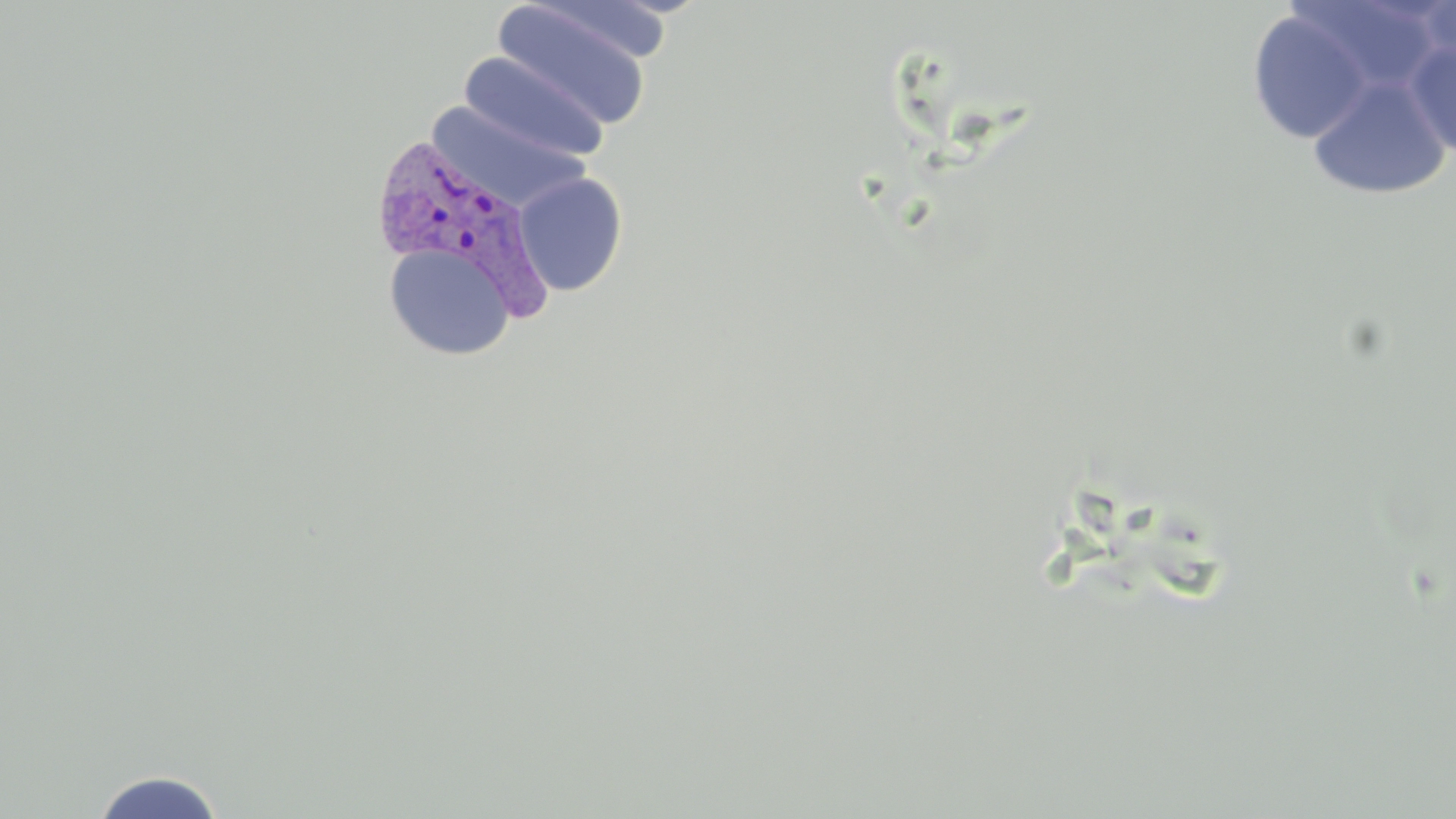
Approximate bounding boxes as named x1/y1/x2/y2 corners in pixels. Plasmodium vivax-infected red blood cell locations: (x1=369, y1=131, x2=558, y2=323). Uninfected red blood cell locations: (x1=1285, y1=0, x2=1446, y2=99), (x1=1414, y1=0, x2=1456, y2=66), (x1=491, y1=3, x2=655, y2=132), (x1=1246, y1=9, x2=1375, y2=145), (x1=1403, y1=39, x2=1456, y2=159), (x1=459, y1=51, x2=611, y2=163), (x1=1307, y1=74, x2=1452, y2=200), (x1=512, y1=171, x2=628, y2=296), (x1=384, y1=243, x2=515, y2=360), (x1=89, y1=769, x2=227, y2=818). Slide-level diagnosis: Plasmodium vivax. Image is 1456×819 pixels. Captured at 1000x magnification. Thin blood smear. Optical microscopy. May-Grünwald-Giemsa stain. One field of a larger specimen.